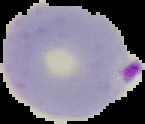

The area outside the segmented cell region is set to black. Malaria status: parasitized. From a thin blood film. Image is 145×124 pixels.